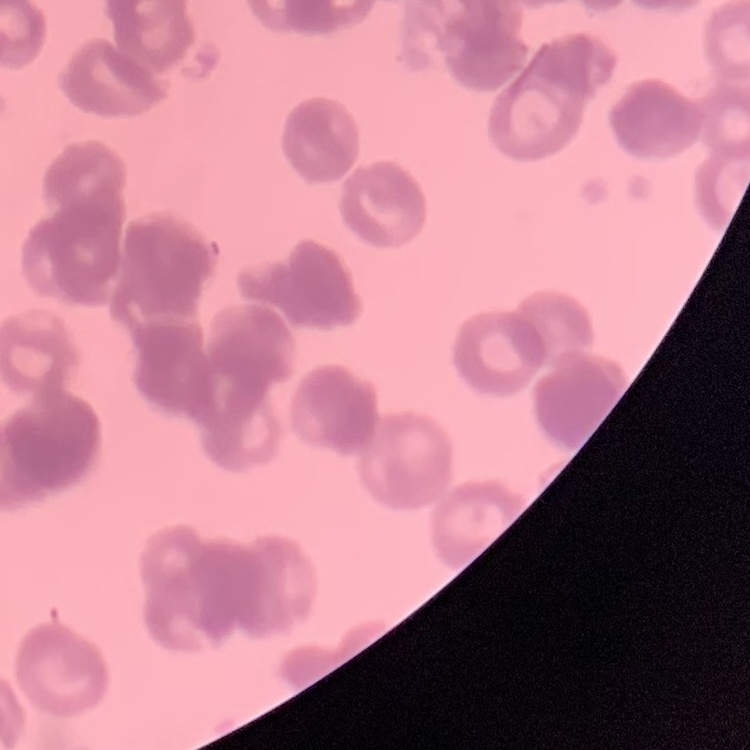
The red blood cells exhibit rouleaux formation. Field's or Giemsa stain. Thin blood smear. One tile cut from a larger photomicrograph.